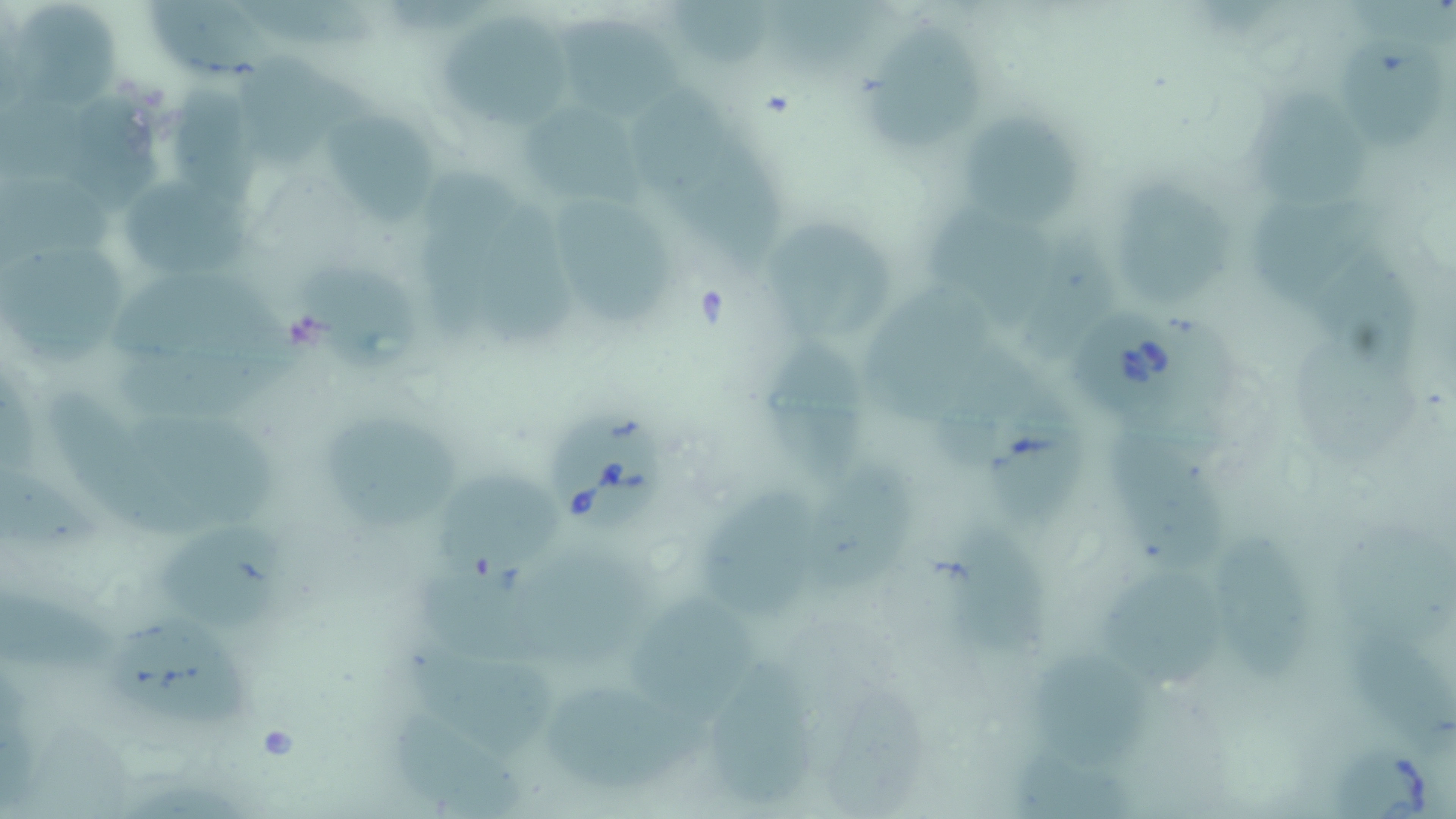

Summary:
  - Coordinate format: approximate bounding boxes as (x1,y1)-(x2,y2) corner pairs in pixels
  - Babesia divergens-infected red blood cell locations: (1075,307)-(1186,424), (551,416)-(665,533), (1323,737)-(1455,819)
  - Uninfected red blood cell locations: (673,0)-(778,66), (149,2)-(272,85), (251,3)-(390,52), (27,9)-(122,117), (566,11)-(697,131), (441,21)-(583,132), (870,26)-(988,156), (1326,37)-(1434,143), (253,61)-(371,170), (177,88)-(271,207), (7,100)-(105,196), (1263,100)-(1377,212), (64,101)-(176,208), (639,101)-(743,218), (531,109)-(669,215), (331,116)-(441,233), (973,116)-(1091,241), (721,149)-(794,281), (428,161)-(532,349), (8,177)-(115,279), (130,181)-(257,281), (1131,185)-(1233,317), (570,195)-(680,338), (1264,199)-(1378,312), (485,203)-(598,349), (940,206)-(1048,326), (1016,222)-(1111,353), (778,234)-(892,338), (5,249)-(131,367), (119,261)-(315,371), (866,265)-(1001,401), (310,270)-(441,387), (768,324)-(870,483), (1294,330)-(1420,458), (131,337)-(320,440), (936,344)-(1044,452), (973,376)-(1085,532), (70,391)-(236,548), (126,404)-(290,519), (327,415)-(465,528), (1129,438)-(1233,568), (3,452)-(117,577), (433,460)-(568,577), (818,464)-(918,596), (717,486)-(827,609), (1323,518)-(1456,640), (168,519)-(306,635), (933,525)-(1055,652), (1229,537)-(1319,683), (550,545)-(669,670), (413,558)-(546,676), (1109,573)-(1225,691), (5,581)-(129,668), (635,600)-(761,721), (1350,611)-(1456,751), (130,621)-(269,734), (403,632)-(554,762), (1039,654)-(1158,754), (713,656)-(820,809), (540,668)-(696,782), (830,680)-(929,813), (389,703)-(521,817), (1009,746)-(1131,819)
  - Slide-level diagnosis: Babesia divergens
  - Preparation: thin blood film
  - Magnification: 1000x
  - Image size: 1456×819 pixels
  - Stain: May-Grünwald-Giemsa
  - Field of view: one of a larger specimen
  - Modality: optical microscopy